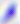

Summary:
  - Magnification: 400x
  - Identification: Toxoplasma gondii
  - Modality: micrograph